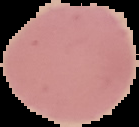
Summary:
  - Result: no malaria parasites detected
  - Image size: 139×127 pixels
  - Image type: segmented cell region with the area outside set to black
  - Preparation: thin blood film